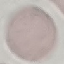
Malaria status: uninfected. Automatically extracted cell patch, resized to 64 × 64 pixels. Giemsa stain. Thin smear of blood. Photographed with a smartphone camera at the microscope eyepiece.